Report the malaria status of this cell.
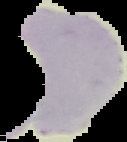

It is uninfected.

{
  "image_type": "cell region segmented out of the field of view; surrounding area masked to black",
  "image_size": "127×142 pixels",
  "preparation": "thin blood film"
}